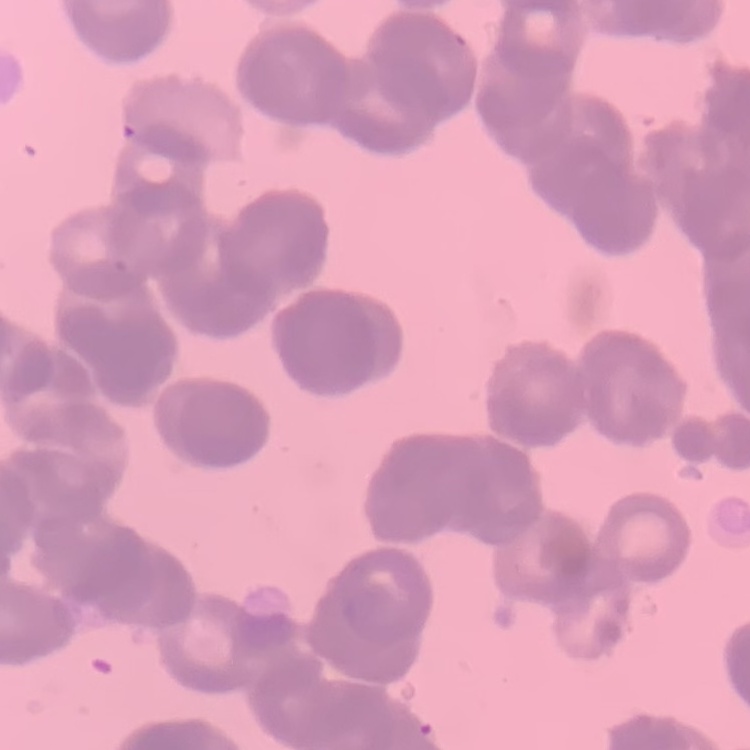

erythrocyte morphology = rouleaux formation
preparation = thin blood film
image type = square crop of a larger photomicrograph
stain = Field's or Giemsa